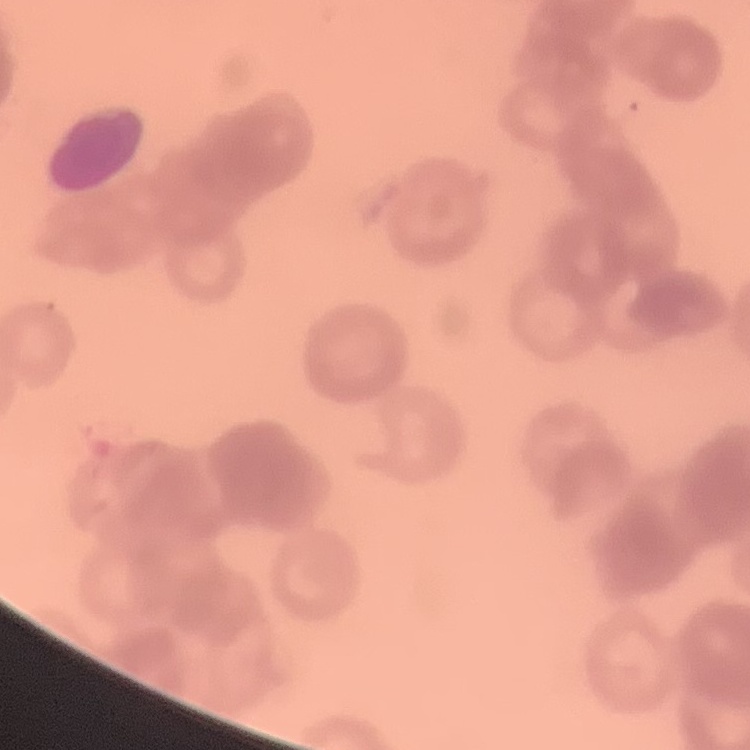 The red blood cells exhibit rouleaux formation. One tile cut from a larger photomicrograph. Field's or Giemsa stain. Thin peripheral smear.